Assess the morphology of the red blood cells.
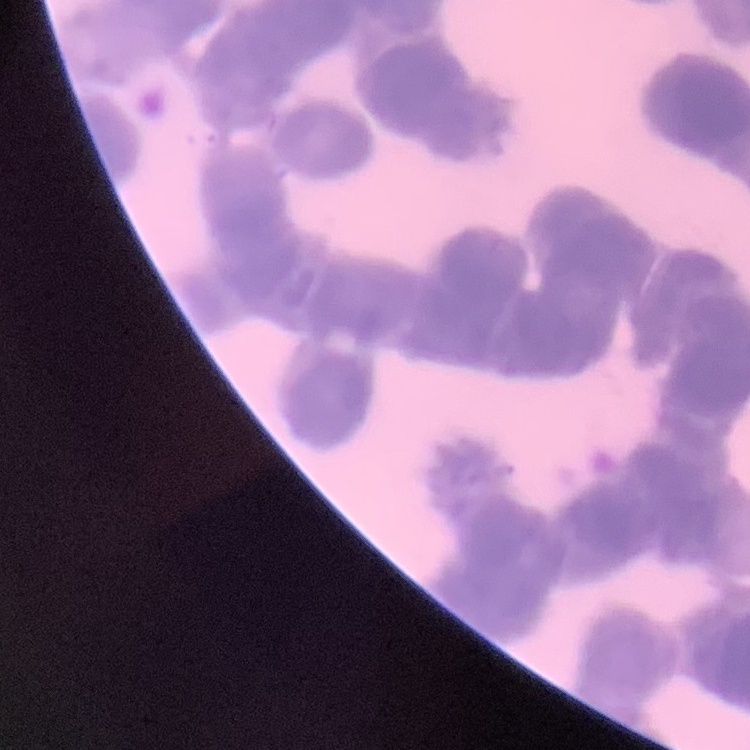

Rouleaux formation.

Summary:
  - Stain: Field's or Giemsa
  - Preparation: thin blood film
  - Image type: one tile cut from a larger photomicrograph